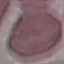
Summary:
  - Result: negative for malaria parasites
  - Capture: smartphone camera at the microscope eyepiece
  - Image type: cell patch, automatically extracted from a larger field of view and resized to 64 × 64 pixels
  - Stain: Giemsa
  - Preparation: thin smear